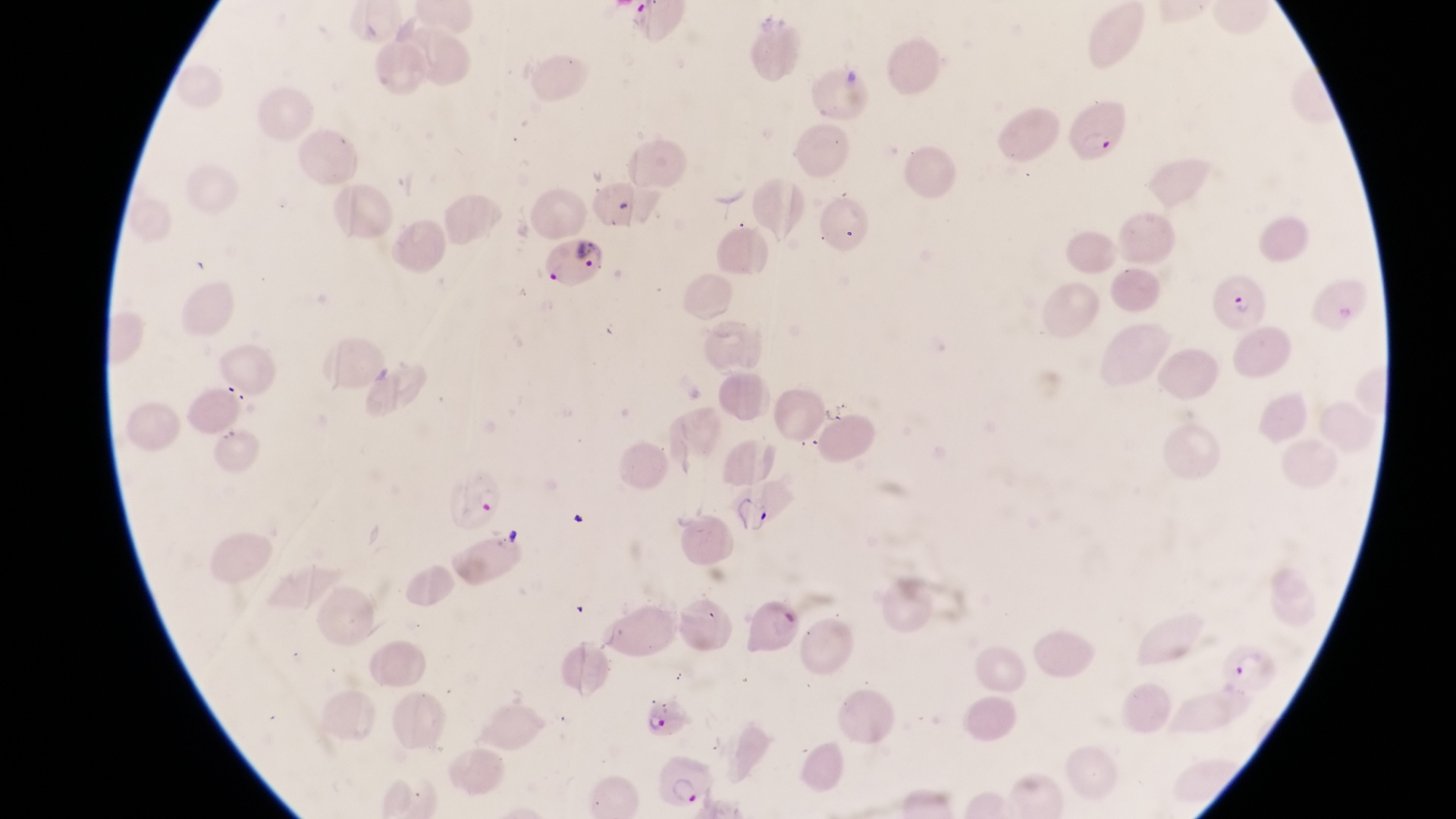
Approximate bounding boxes as [left, top, right, bottom] in pixels.
Summary:
  - Parasitised red blood cell locations: [1067, 98, 1130, 170], [541, 234, 608, 286], [1218, 275, 1270, 330], [442, 469, 514, 533], [639, 695, 698, 738], [658, 753, 714, 811]
  - Magnification: 1000x
  - Preparation: thin blood smear
  - Image size: 1456×819 pixels
  - Field of view: single
  - Country: Uganda
  - Capture: smartphone photograph through the eyepiece of an Olympus CX-23 microscope